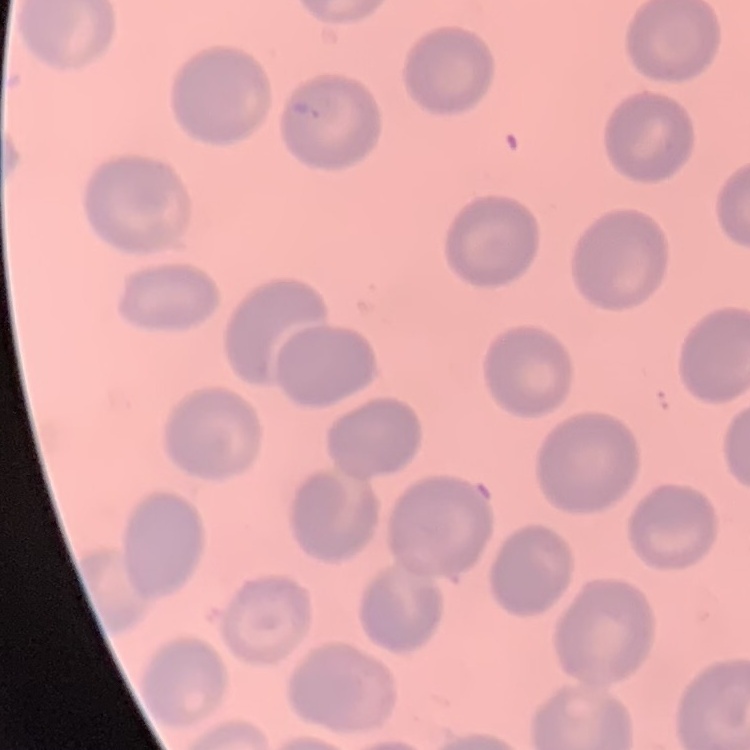

erythrocyte_morphology: no rouleaux formation
stain: Field's or Giemsa
image_type: square crop of a larger photomicrograph
preparation: thin blood smear